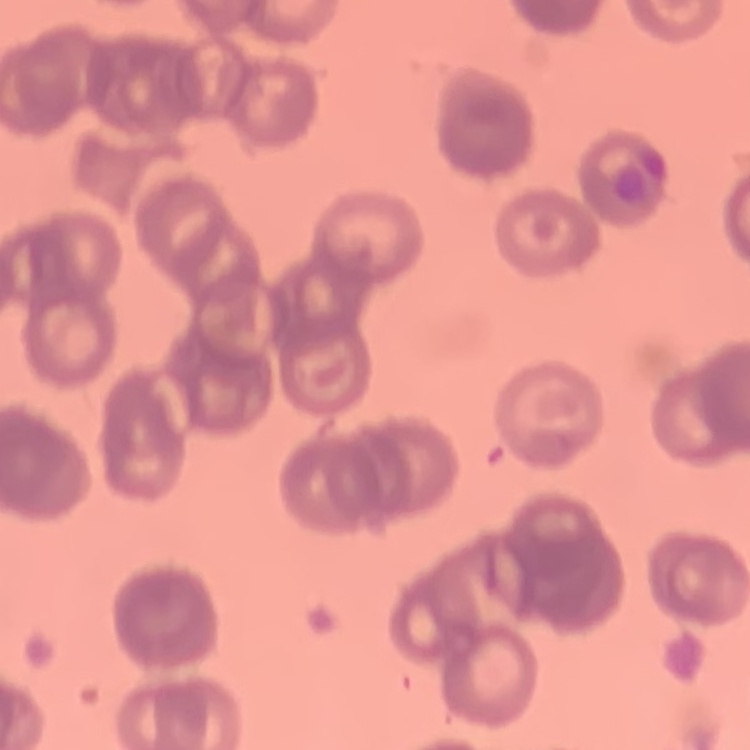
red blood cell morphology = rouleaux formation
preparation = thin peripheral smear
stain = Field's or Giemsa
image type = square crop of a larger photomicrograph